Classify this cell by malaria status.
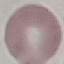
It is uninfected.

Thin blood smear. Automatically extracted cell patch, resized to 64 × 64 pixels. Giemsa-stained preparation. Photographed with a smartphone camera at the microscope eyepiece.